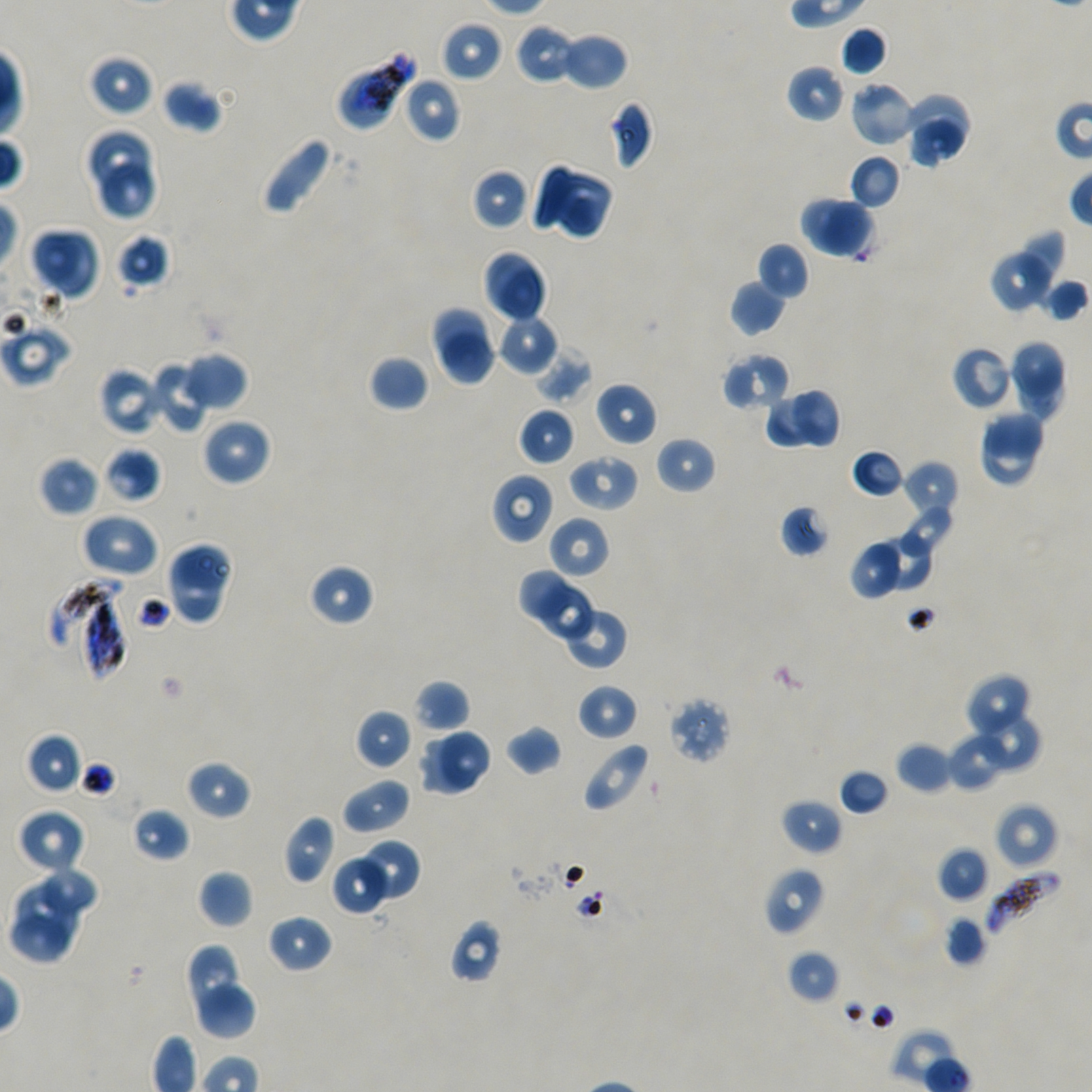
Approximate bounding rectangles given as corner coordinates in pixels from the top-left. Not every red blood cell is marked. Locations of infected red blood cells: (x1=50, y1=579, x2=125, y2=647), (x1=84, y1=598, x2=125, y2=679), (x1=987, y1=871, x2=1062, y2=935). Locations of uninfected red blood cells: (x1=439, y1=20, x2=503, y2=82), (x1=515, y1=24, x2=576, y2=85), (x1=840, y1=25, x2=888, y2=76), (x1=560, y1=32, x2=629, y2=92), (x1=88, y1=54, x2=154, y2=116), (x1=786, y1=65, x2=846, y2=123), (x1=402, y1=77, x2=461, y2=143), (x1=162, y1=79, x2=223, y2=133), (x1=849, y1=81, x2=917, y2=147), (x1=904, y1=94, x2=974, y2=151), (x1=607, y1=101, x2=653, y2=170), (x1=908, y1=118, x2=966, y2=169), (x1=86, y1=128, x2=151, y2=189), (x1=260, y1=135, x2=337, y2=218), (x1=848, y1=153, x2=902, y2=210), (x1=99, y1=164, x2=160, y2=220), (x1=533, y1=164, x2=615, y2=240), (x1=470, y1=168, x2=530, y2=230), (x1=801, y1=195, x2=875, y2=258), (x1=30, y1=227, x2=84, y2=287), (x1=1019, y1=227, x2=1064, y2=308), (x1=48, y1=231, x2=99, y2=302), (x1=116, y1=233, x2=170, y2=290), (x1=756, y1=241, x2=809, y2=300), (x1=989, y1=249, x2=1053, y2=313), (x1=482, y1=250, x2=549, y2=323), (x1=1040, y1=276, x2=1089, y2=322), (x1=729, y1=280, x2=787, y2=336), (x1=431, y1=308, x2=487, y2=366), (x1=496, y1=315, x2=558, y2=375), (x1=1, y1=321, x2=72, y2=386), (x1=437, y1=330, x2=498, y2=387), (x1=1007, y1=341, x2=1063, y2=399), (x1=951, y1=345, x2=1013, y2=411), (x1=536, y1=346, x2=594, y2=403), (x1=182, y1=352, x2=247, y2=412), (x1=722, y1=353, x2=790, y2=412), (x1=369, y1=354, x2=430, y2=412), (x1=147, y1=361, x2=211, y2=433), (x1=98, y1=365, x2=166, y2=435), (x1=1018, y1=366, x2=1064, y2=422), (x1=594, y1=382, x2=657, y2=446), (x1=790, y1=386, x2=841, y2=451), (x1=764, y1=395, x2=820, y2=450), (x1=517, y1=407, x2=575, y2=466), (x1=982, y1=410, x2=1045, y2=458), (x1=202, y1=417, x2=271, y2=486), (x1=977, y1=428, x2=1037, y2=488), (x1=655, y1=436, x2=716, y2=494), (x1=103, y1=447, x2=161, y2=504), (x1=852, y1=448, x2=905, y2=498), (x1=566, y1=453, x2=639, y2=513), (x1=39, y1=456, x2=98, y2=517), (x1=902, y1=460, x2=960, y2=520), (x1=491, y1=473, x2=555, y2=543), (x1=898, y1=503, x2=956, y2=558), (x1=779, y1=504, x2=830, y2=558), (x1=80, y1=513, x2=158, y2=578), (x1=547, y1=515, x2=611, y2=580), (x1=873, y1=535, x2=934, y2=590), (x1=851, y1=539, x2=899, y2=598), (x1=170, y1=540, x2=234, y2=594), (x1=165, y1=551, x2=228, y2=624), (x1=308, y1=564, x2=375, y2=627), (x1=517, y1=570, x2=572, y2=624), (x1=540, y1=584, x2=595, y2=643), (x1=565, y1=611, x2=627, y2=670), (x1=963, y1=672, x2=1032, y2=739), (x1=414, y1=679, x2=469, y2=733), (x1=577, y1=683, x2=638, y2=741), (x1=666, y1=697, x2=731, y2=765), (x1=355, y1=708, x2=414, y2=770), (x1=966, y1=710, x2=1041, y2=774), (x1=505, y1=725, x2=563, y2=776), (x1=440, y1=729, x2=490, y2=790), (x1=947, y1=730, x2=1006, y2=790), (x1=25, y1=733, x2=82, y2=795), (x1=420, y1=735, x2=475, y2=796), (x1=581, y1=741, x2=651, y2=814), (x1=896, y1=742, x2=954, y2=795), (x1=185, y1=759, x2=251, y2=820), (x1=838, y1=769, x2=890, y2=816), (x1=341, y1=776, x2=411, y2=835), (x1=780, y1=798, x2=843, y2=856), (x1=994, y1=802, x2=1059, y2=869), (x1=132, y1=807, x2=189, y2=862), (x1=18, y1=809, x2=86, y2=875), (x1=283, y1=814, x2=336, y2=884), (x1=358, y1=839, x2=421, y2=903), (x1=936, y1=846, x2=989, y2=902), (x1=331, y1=853, x2=392, y2=915), (x1=39, y1=866, x2=101, y2=915), (x1=763, y1=867, x2=825, y2=936), (x1=197, y1=869, x2=253, y2=928), (x1=15, y1=882, x2=79, y2=946), (x1=9, y1=912, x2=70, y2=962), (x1=267, y1=914, x2=333, y2=972), (x1=943, y1=915, x2=987, y2=966), (x1=448, y1=919, x2=504, y2=984), (x1=185, y1=946, x2=240, y2=1011), (x1=786, y1=949, x2=840, y2=1004), (x1=197, y1=983, x2=256, y2=1040). Locations of red blood cells of indeterminate infection status: (x1=335, y1=48, x2=415, y2=131). Plasmodium falciparum strain NF54 in static in-vitro culture. Donor blood group A+/O+. One field from this slide. Image is 1092×1092 pixels. Thin blood film. Giemsa-stained preparation. Oil immersion, 100x objective (numerical aperture 1.45).